Assess for malaria.
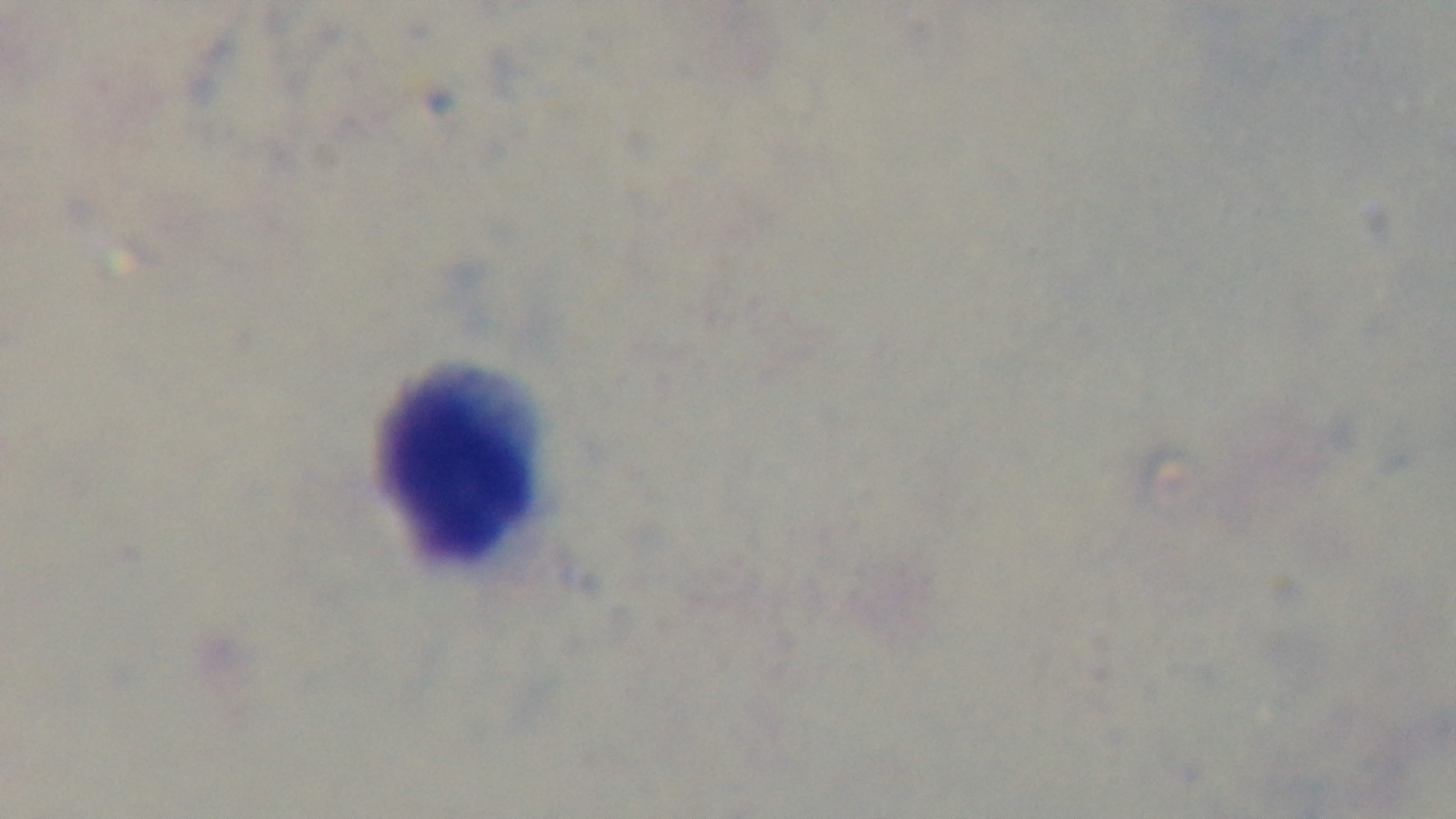

Uninfected.

Preparation: thick smear. Photomicrograph. Single field of view. Giemsa-stained. 100x oil-immersion objective. Mounted 4K digital camera.